Name the parasite shown.
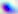

This is Toxoplasma gondii.

magnification = 400x
modality = micrograph